Assess the morphology of the red blood cells.
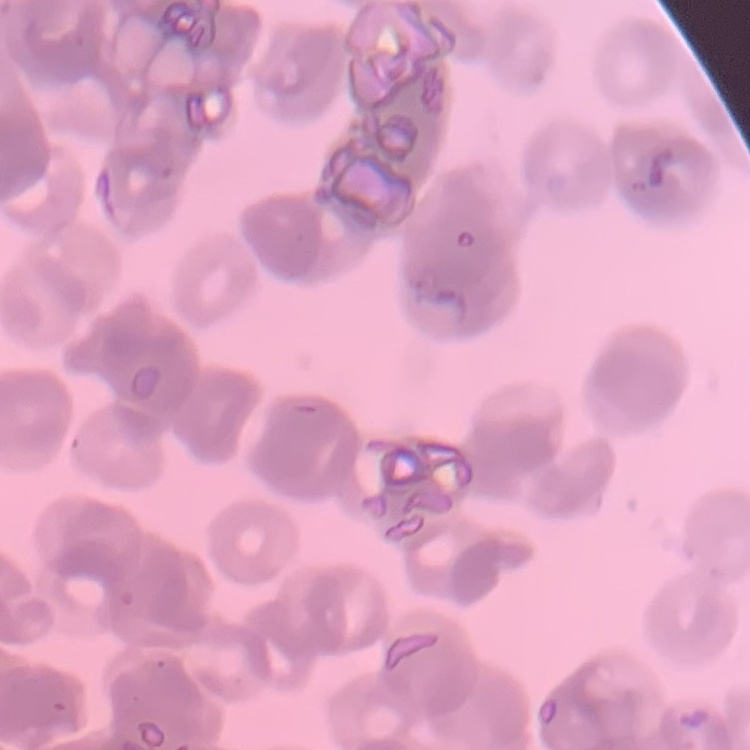
Rouleaux formation.

stain = Field's or Giemsa
preparation = thin blood film
image type = one tile cut from a larger photomicrograph